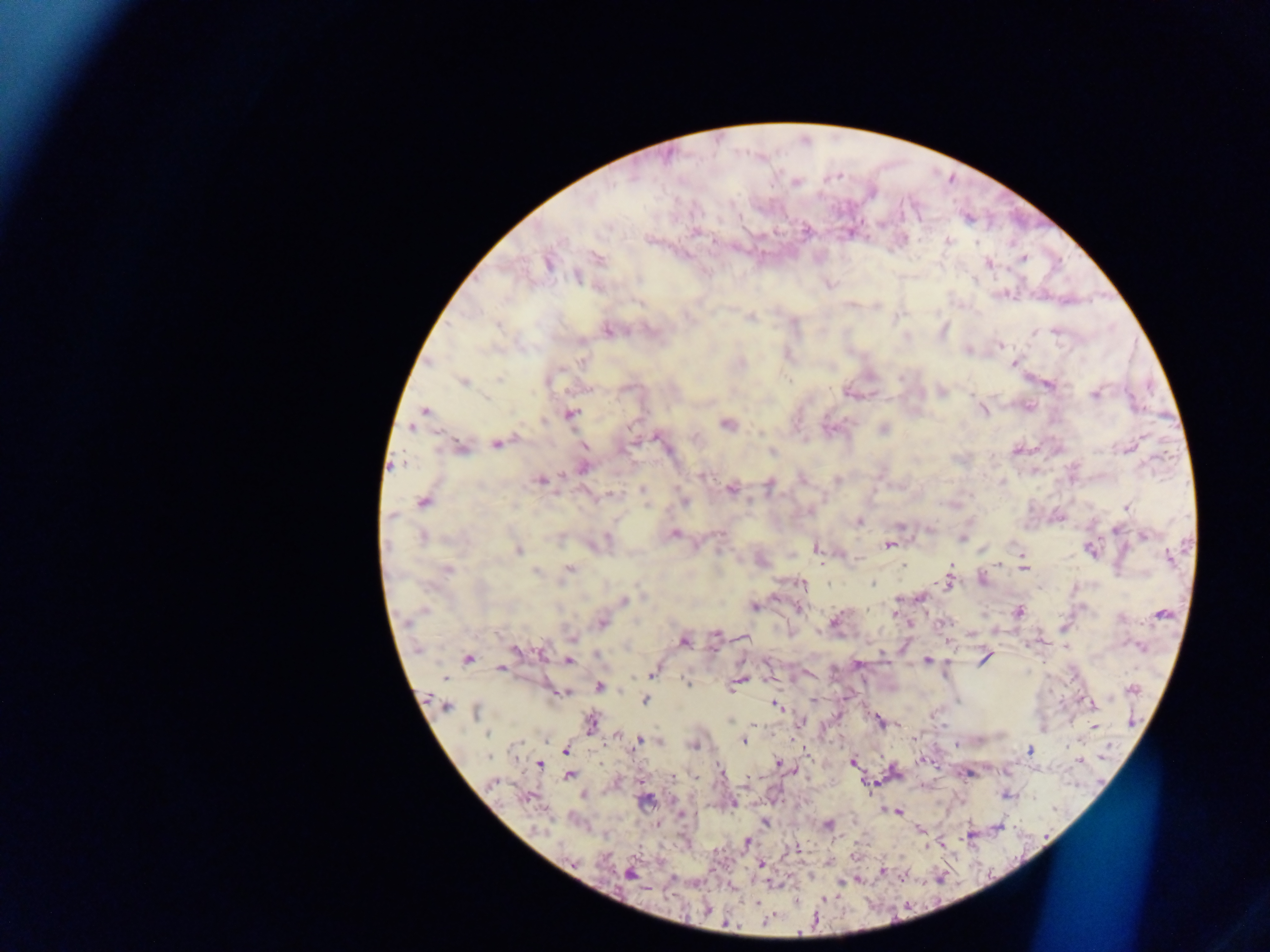
image size = 1270×952 pixels
country = Ghana
preparation = thick blood film
field of view = single
malaria parasite locations = approximate centers as [x, y] in pixels: [796, 182], [695, 231], [948, 241], [598, 258], [1023, 258], [989, 262], [548, 263], [577, 277], [639, 303], [750, 318], [498, 326], [608, 331], [1055, 331], [1034, 333], [1000, 345], [967, 351], [581, 362], [1012, 364], [499, 379], [463, 382], [547, 382], [1049, 385], [941, 391], [1095, 395], [982, 410], [424, 411], [570, 415], [543, 421], [728, 424], [883, 430], [695, 436], [658, 438], [496, 444], [584, 446], [462, 448], [772, 453], [583, 468], [702, 476], [837, 479], [541, 480], [769, 486], [642, 489], [731, 489], [610, 493], [423, 501], [684, 501], [1126, 508], [392, 516], [859, 522], [900, 526], [1115, 530], [675, 533], [1144, 535], [607, 537], [422, 538], [962, 539], [888, 546], [817, 548], [518, 550], [1091, 550], [982, 551], [1022, 555], [1169, 558], [857, 560], [999, 564], [903, 565], [952, 565], [570, 568], [1024, 568], [447, 570], [536, 572], [948, 583], [802, 584], [872, 584], [921, 598], [624, 600], [754, 606], [798, 608], [1018, 611], [894, 613], [1162, 613], [835, 620], [601, 623], [716, 634], [572, 638], [745, 638], [684, 642], [516, 651], [542, 652], [984, 658], [468, 659], [927, 660], [569, 661], [500, 668], [652, 672], [738, 681], [686, 682], [599, 686], [1133, 689], [561, 692], [646, 700], [445, 705], [775, 705], [1091, 705], [476, 712], [879, 721], [591, 723], [1094, 726], [487, 734], [637, 741], [743, 741], [694, 746], [1030, 750], [566, 751], [488, 757], [852, 762], [778, 763], [539, 765], [570, 775], [673, 777], [493, 783], [645, 801], [732, 804], [897, 812], [765, 822], [828, 825], [919, 829], [747, 842], [797, 849], [761, 864], [883, 871], [630, 874], [757, 902], [766, 921], [726, 924]
capture = mobile-phone photograph through a microscope